Describe the morphology of the erythrocytes.
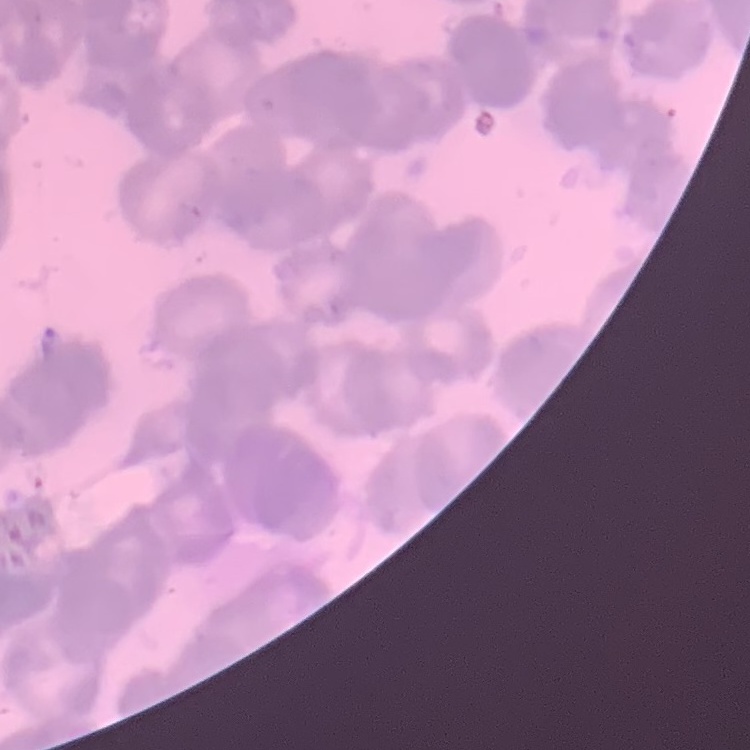

Rouleaux formation.

stain = Field's or Giemsa
preparation = thin peripheral smear
image type = square crop of a larger photomicrograph